Assess the morphology of the erythrocytes.
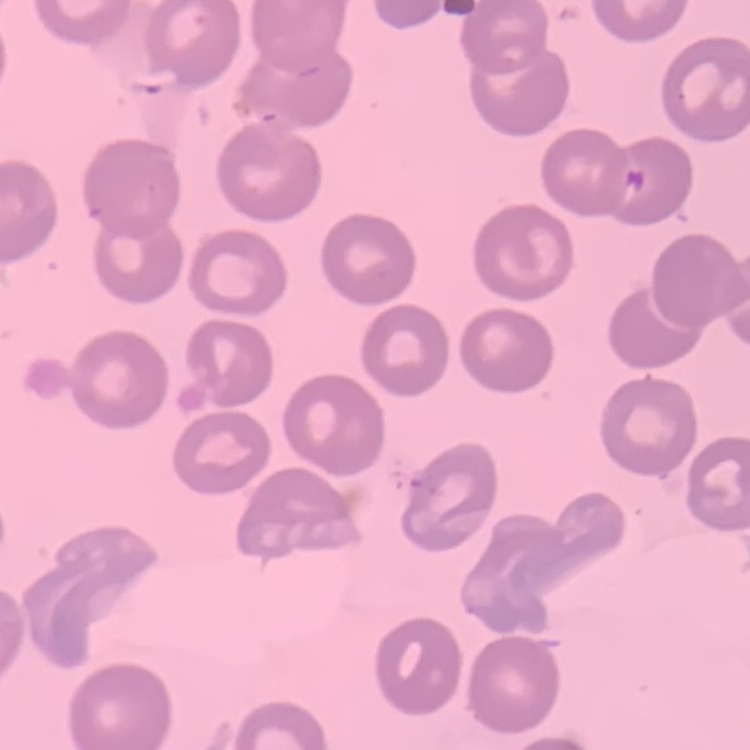

No rouleaux formation.

Thin blood film. Field's or Giemsa stain. One tile cut from a larger photomicrograph.